Comment on the morphology of the red blood cells.
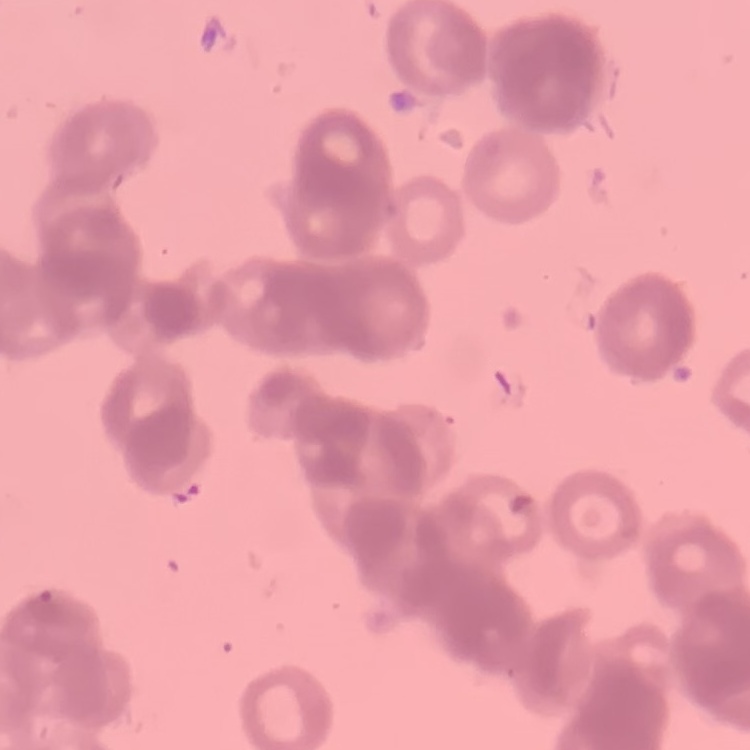
They show rouleaux formation.

Summary:
  - Stain: Field's or Giemsa
  - Image type: square crop of a larger photomicrograph
  - Preparation: thin peripheral smear